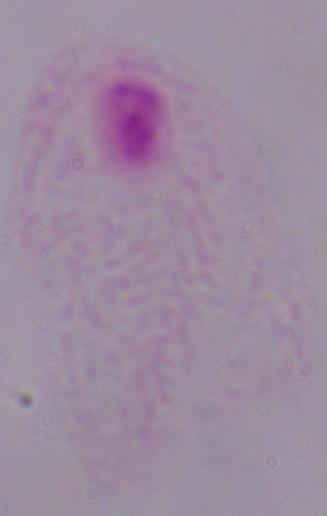

modality = micrograph
identification = trichomonad
magnification = 1000x